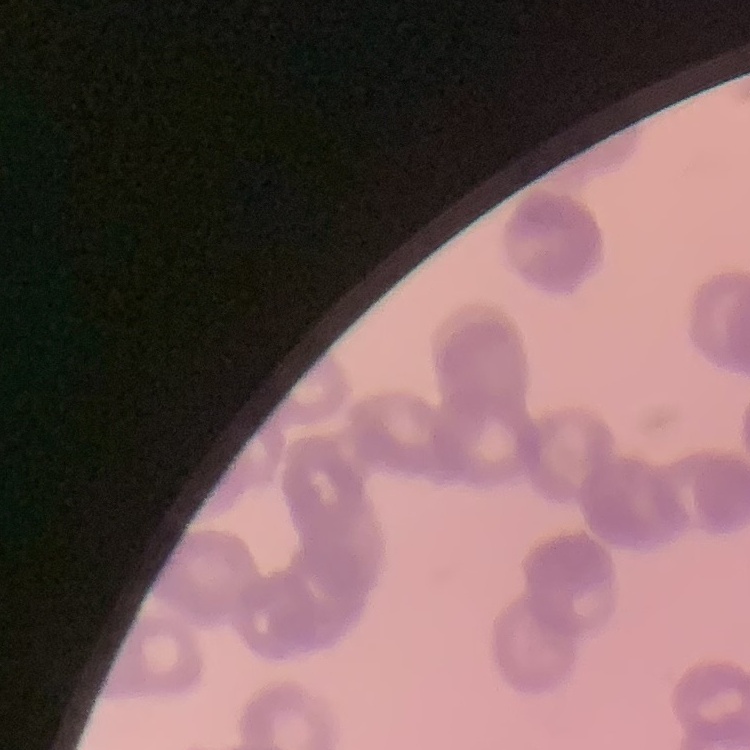
erythrocyte morphology = rouleaux formation
image type = one tile cut from a larger photomicrograph
stain = Field's or Giemsa
preparation = thin blood film